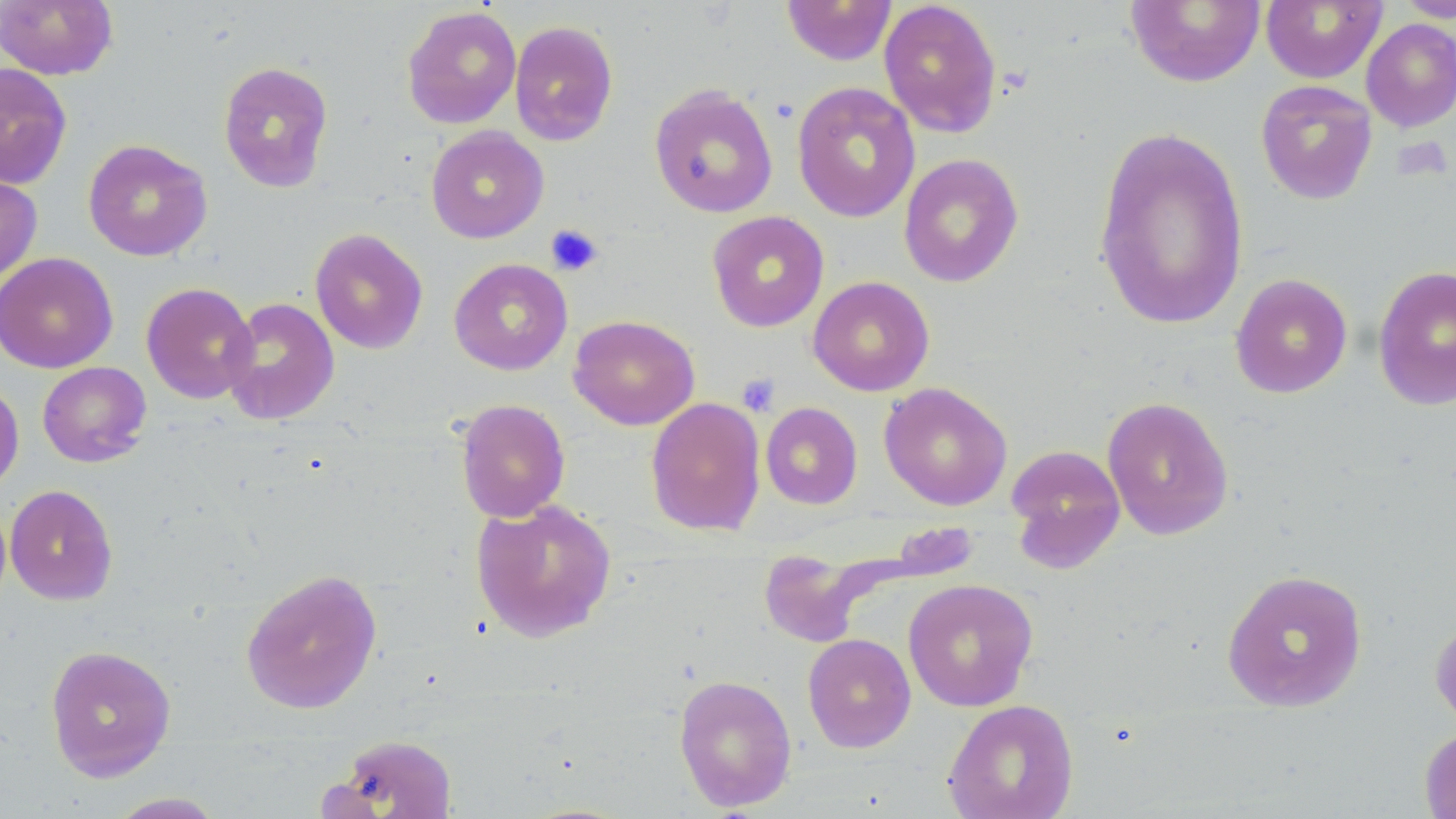
Summary:
  - Coordinate format: approximate bounding boxes as (x1,y1)-(x2,y2) corner pairs in pixels
  - Platelet locations: (545,224)-(603,276), (736,374)-(780,416)
  - Uninfected red blood cell locations: (0,0)-(118,80), (781,0)-(897,66), (878,0)-(1002,137), (1125,0)-(1266,88), (1260,0)-(1386,84), (1393,0)-(1456,22), (402,5)-(522,129), (1361,18)-(1456,132), (509,20)-(618,146), (217,60)-(334,192), (0,63)-(72,189), (1255,80)-(1378,205), (792,82)-(921,223), (648,84)-(778,218), (1092,124)-(1250,330), (425,126)-(549,243), (83,139)-(212,261), (898,153)-(1024,288), (0,172)-(42,284), (706,211)-(830,332), (310,228)-(429,354), (0,252)-(117,373), (449,257)-(573,375), (1373,264)-(1456,411), (1230,273)-(1352,398), (808,276)-(935,396), (140,282)-(258,404), (221,297)-(340,425), (568,314)-(700,431), (37,361)-(151,467), (0,377)-(24,494), (879,381)-(1012,511), (1102,396)-(1234,540), (645,397)-(766,537), (455,398)-(570,522), (760,402)-(863,509), (1005,444)-(1125,572), (5,484)-(118,605), (470,498)-(618,642), (759,549)-(869,647), (240,568)-(383,714), (1222,569)-(1368,712), (902,578)-(1039,712), (1430,616)-(1456,734), (802,633)-(916,753), (45,644)-(176,781), (673,673)-(797,811), (943,698)-(1079,819), (1420,727)-(1456,819), (331,733)-(459,818), (106,792)-(226,818)
  - Slide-level diagnosis: negative for blood parasites
  - Magnification: 1000x
  - Preparation: thin blood film
  - Field of view: one of a larger specimen
  - Image size: 1456×819 pixels
  - Modality: optical microscopy
  - Stain: May-Grünwald-Giemsa